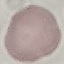

Result: negative for malaria parasites. Giemsa-stained preparation. Acquired by smartphone through the microscope eyepiece. Thin blood film. Cell patch, automatically extracted from a larger field of view and resized to 64 × 64 pixels.